Point out each malaria parasite and each leukocyte.
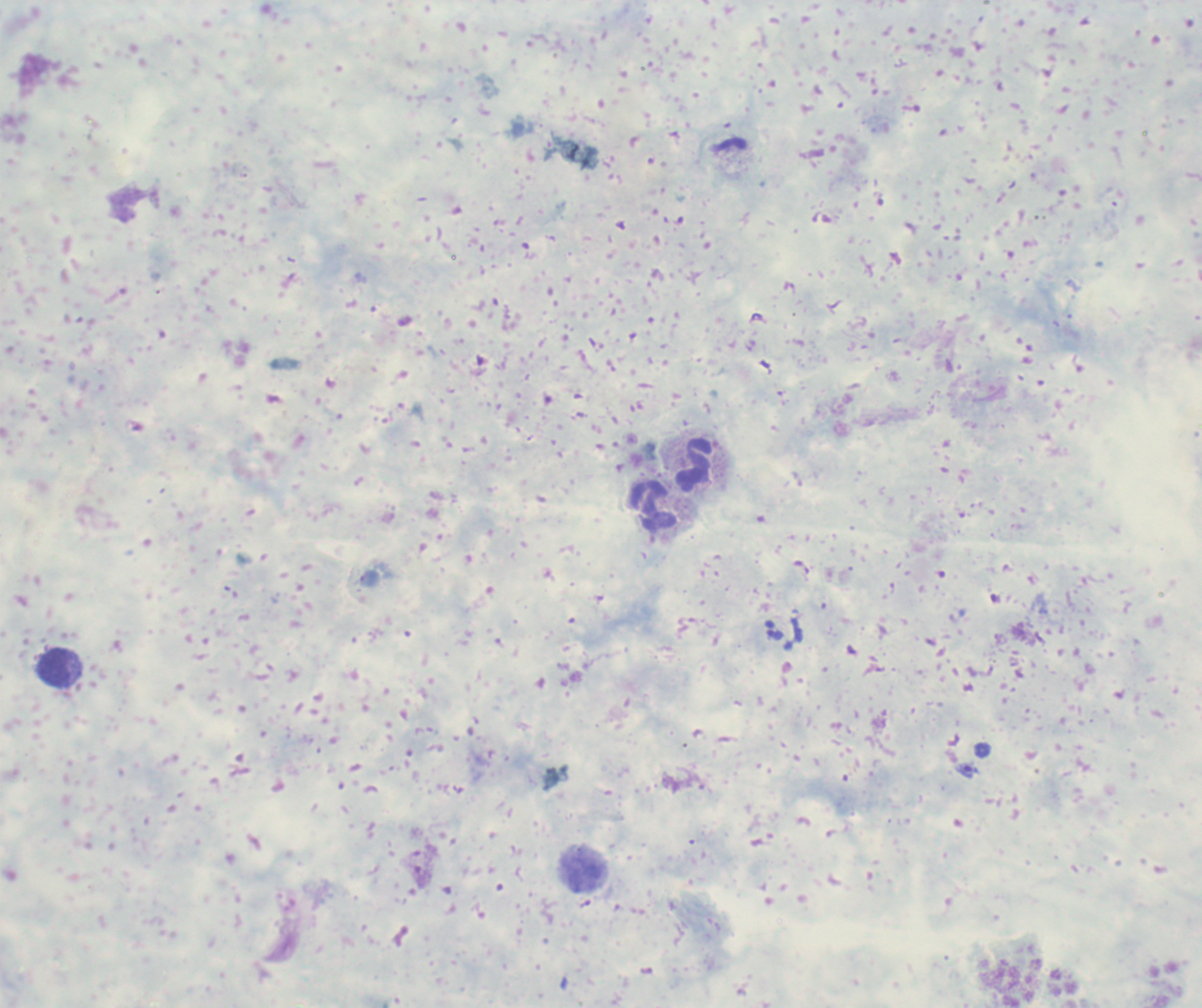
Approximate object centers, in pixels from the top-left corner.
Trophozoites: (x=774, y=630), (x=968, y=770).
No schizont or gametocyte forms observed.
Leukocytes: (x=695, y=465), (x=653, y=506), (x=53, y=668), (x=583, y=873).

Summary:
  - Context: previously used in an actual diagnosis
  - Magnification: 100x
  - Stain: Romanowsky
  - Image size: 1202×1008 pixels
  - Preparation: thick smear of blood
  - Background quality: unsatisfactory
  - Field of view: single